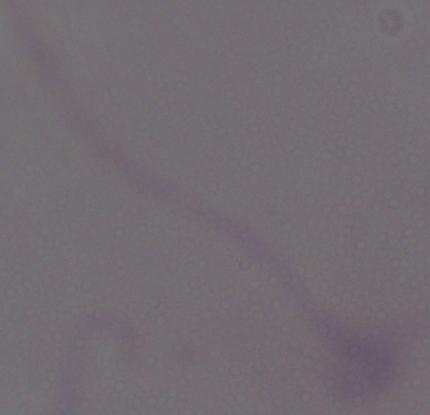

Photomicrograph. 1000x magnification. A Leishmania parasite is shown.